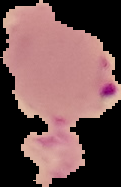
Summary:
  - Image type: cell region segmented out of the field of view; surrounding area masked to black
  - Malaria status: parasitized
  - Image size: 121×187 pixels
  - Preparation: thin blood smear